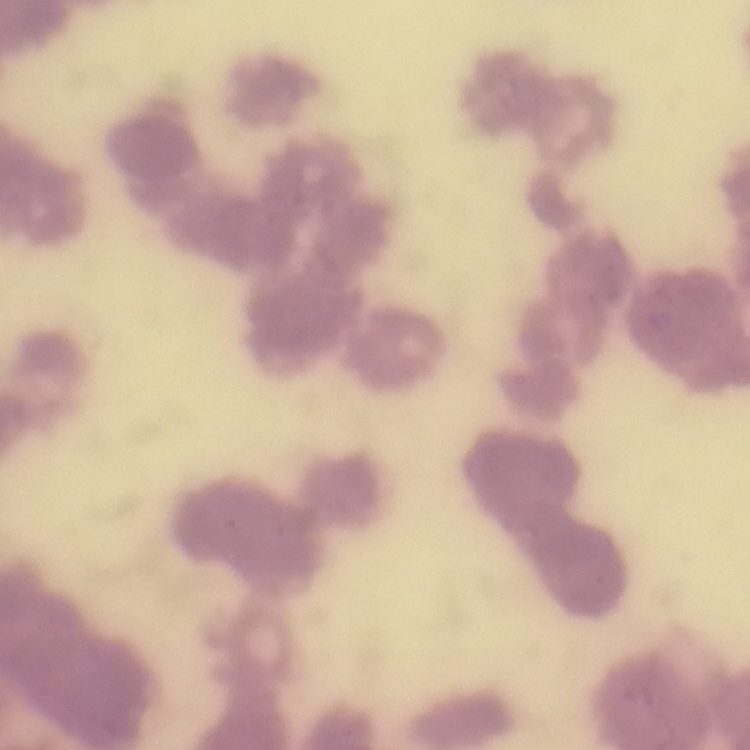

red blood cell morphology = rouleaux formation
stain = Field's or Giemsa
image type = square crop of a larger photomicrograph
preparation = thin blood film